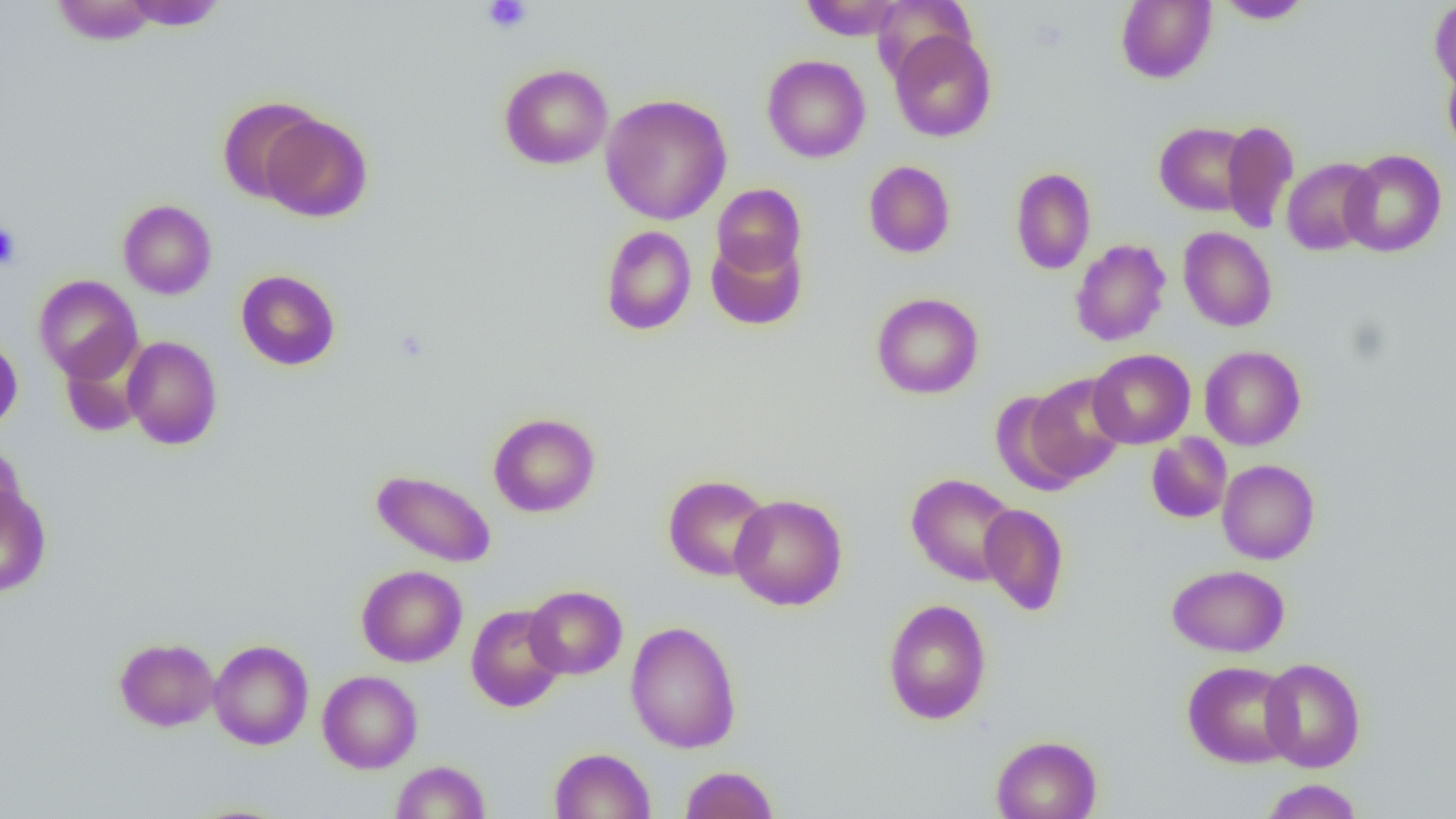

Approximate bounding boxes as (x1,y1)-(x2,y2) corner pairs in pixels. Uninfected red blood cell locations: (801,0)-(904,41), (1115,0)-(1216,84), (1429,0)-(1456,93), (52,1)-(159,45), (120,1)-(228,31), (1215,1)-(1314,24), (889,30)-(996,142), (762,54)-(870,163), (1443,61)-(1456,157), (499,63)-(613,169), (600,94)-(732,225), (217,96)-(322,203), (259,113)-(372,222), (1221,120)-(1299,234), (1154,122)-(1253,215), (1340,149)-(1447,257), (1281,157)-(1379,256), (863,160)-(956,258), (1010,167)-(1096,275), (711,183)-(806,278), (118,199)-(217,299), (600,225)-(696,335), (1178,227)-(1277,332), (706,235)-(806,331), (1070,239)-(1171,347), (236,269)-(340,371), (33,274)-(143,383), (871,292)-(984,399), (0,336)-(22,433), (122,336)-(223,449), (60,343)-(147,437), (1199,345)-(1306,450), (1088,349)-(1196,448), (1025,374)-(1129,484), (989,389)-(1088,494), (488,413)-(600,517), (1146,433)-(1232,524), (0,443)-(27,536), (1217,459)-(1320,564), (371,469)-(496,568), (906,473)-(1019,586), (663,474)-(773,581), (0,486)-(51,597), (728,493)-(847,611), (979,503)-(1069,616), (1167,564)-(1290,657), (356,565)-(467,667), (524,585)-(627,679), (882,598)-(992,725), (466,604)-(567,712), (625,620)-(742,753), (114,637)-(220,732), (208,639)-(313,750), (1259,658)-(1366,772), (1182,660)-(1298,768), (317,670)-(422,773), (990,734)-(1102,819), (549,747)-(655,819), (391,760)-(490,818), (680,765)-(779,819), (1259,779)-(1364,818). Platelet locations: (482,0)-(532,34), (0,222)-(21,269). Slide-level diagnosis: negative for blood parasites. Captured at 1000x magnification. One field of a larger specimen. Thin blood film. Light microscopy. Image is 1456×819 pixels.